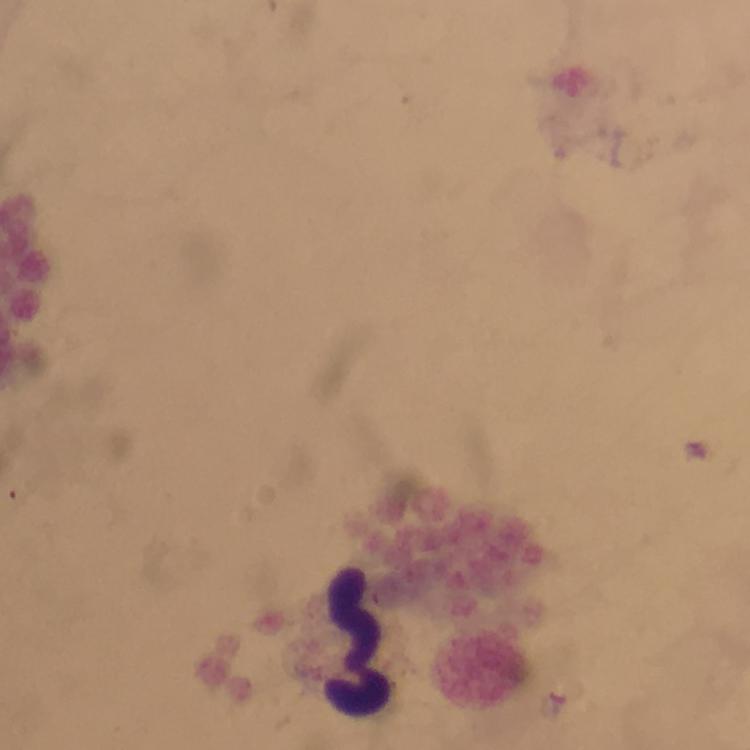 Approximate centers as (x, y) in pixels. Leukocyte locations: (356, 641). Smartphone photograph taken through a microscope. Malaria parasites: none detected. Giemsa stain. Cropped region of a single field of view. At 100x magnification. Thick blood smear. Immersion oil was used. From a malaria diagnostic workup. Image is 750×750 pixels.